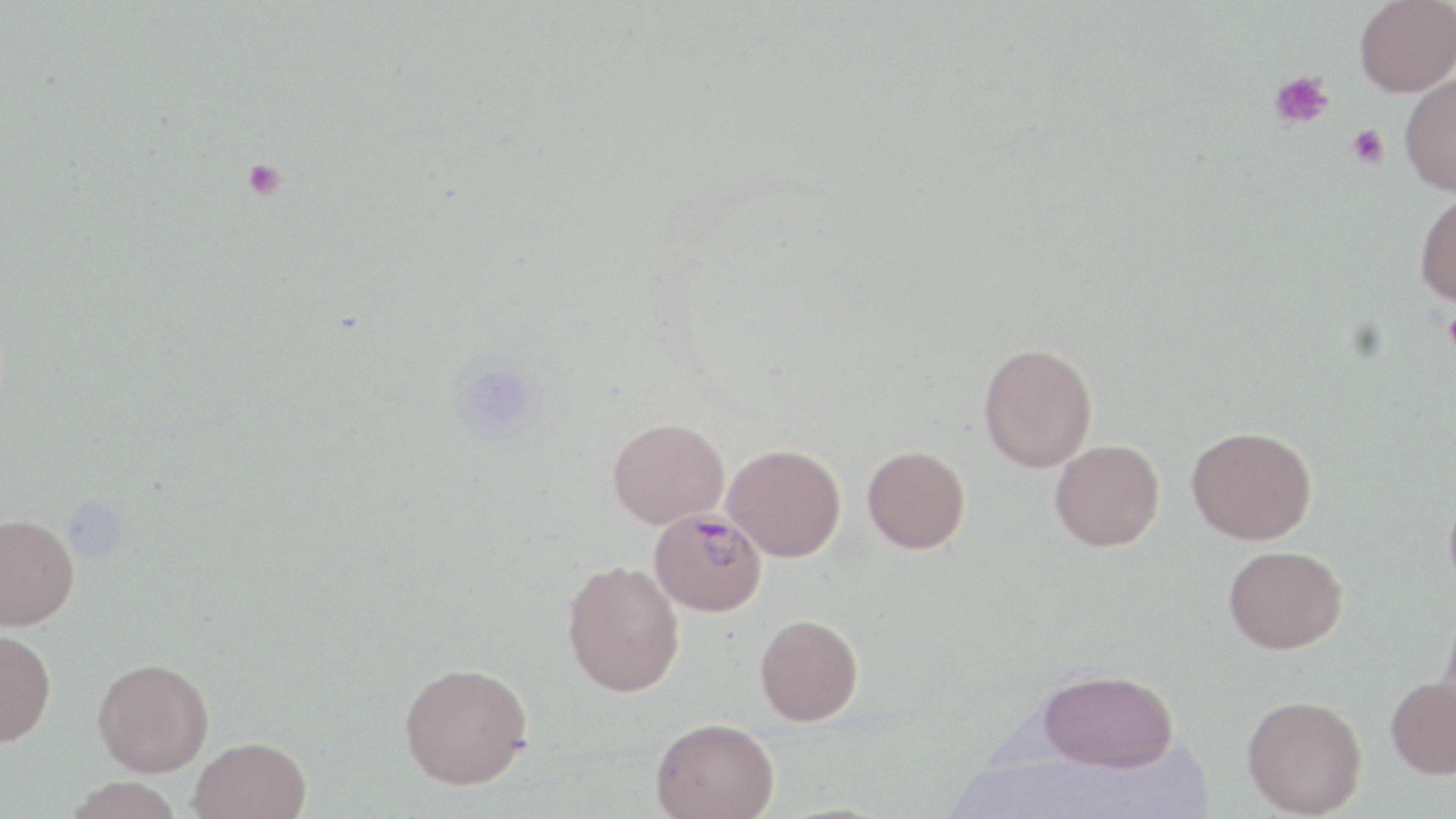

Summary:
  - Coordinate format: approximate bounding boxes as (x1, y1, x2, y2) in pixels
  - Uninfected red blood cell locations: (1355, 0, 1456, 97), (1399, 72, 1456, 196), (1414, 191, 1456, 306), (978, 343, 1098, 473), (607, 416, 729, 528), (1186, 425, 1317, 545), (1050, 439, 1165, 551), (723, 443, 846, 562), (862, 445, 970, 554), (1443, 482, 1456, 604), (0, 513, 80, 630), (1223, 545, 1348, 653), (561, 560, 685, 698), (754, 614, 864, 726), (0, 629, 57, 747), (92, 657, 214, 776), (399, 661, 533, 789), (1036, 668, 1180, 772), (1385, 674, 1456, 779), (1242, 694, 1367, 818), (650, 717, 779, 819), (188, 736, 312, 819), (64, 777, 184, 819)
  - Platelet locations: (1269, 70, 1334, 130), (1345, 124, 1389, 169), (242, 158, 287, 201), (1441, 309, 1456, 353)
  - Plasmodium malariae-infected red blood cell locations: (649, 508, 766, 616)
  - Slide-level diagnosis: Plasmodium malariae
  - Magnification: 1000x
  - Modality: light microscopy
  - Stain: May-Grünwald-Giemsa
  - Preparation: thin blood film
  - Image size: 1456×819 pixels
  - Field of view: one of a larger specimen